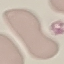

Malaria status: uninfected. Acquired by smartphone through the microscope eyepiece. Cell patch, automatically extracted from a larger field of view and resized to 64 × 64 pixels. Thin blood smear. Giemsa-stained preparation.